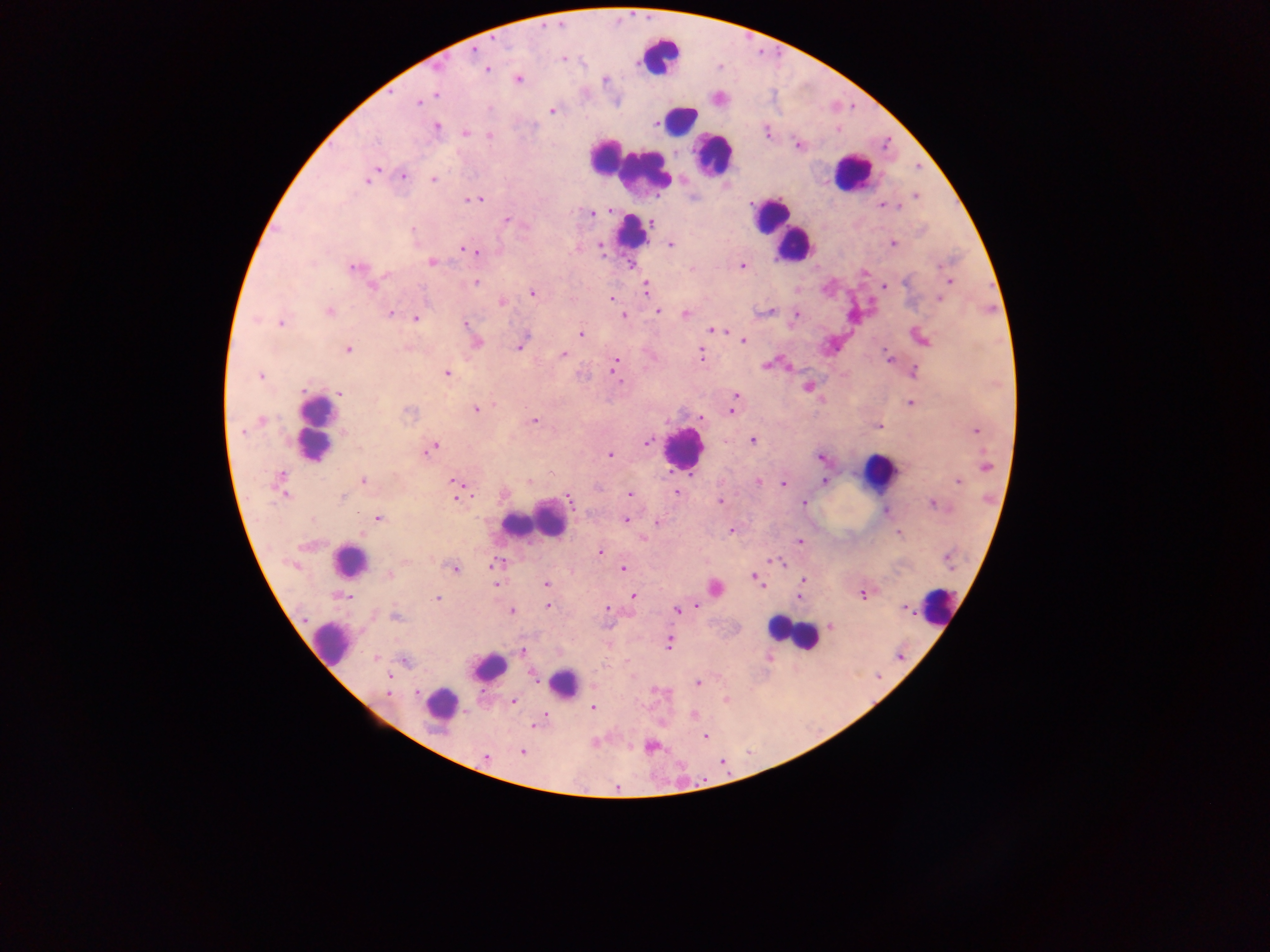
Approximate centers as {x, y} in pixels.
Summary:
  - Leukocyte locations: {660, 56}, {679, 119}, {712, 154}, {609, 157}, {637, 169}, {852, 173}, {770, 214}, {781, 229}, {632, 233}, {793, 245}, {316, 428}, {683, 448}, {878, 472}, {546, 517}, {513, 524}, {349, 561}, {938, 606}, {792, 634}, {329, 642}, {489, 666}, {563, 683}, {440, 704}
  - Plasmodium parasite locations: {474, 50}, {564, 59}, {438, 68}, {486, 69}, {604, 79}, {519, 80}, {437, 96}, {418, 103}, {489, 109}, {552, 110}, {436, 127}, {766, 131}, {464, 133}, {489, 135}, {798, 145}, {377, 168}, {371, 175}, {403, 175}, {433, 179}, {367, 181}, {915, 197}, {466, 199}, {476, 199}, {884, 205}, {896, 207}, {610, 211}, {598, 213}, {592, 214}, {506, 220}, {651, 222}, {413, 230}, {671, 244}, {893, 244}, {601, 246}, {463, 250}, {475, 252}, {431, 262}, {631, 265}, {742, 266}, {355, 268}, {863, 271}, {949, 281}, {475, 283}, {372, 285}, {885, 286}, {646, 288}, {532, 293}, {611, 298}, {939, 298}, {502, 302}, {329, 311}, {658, 311}, {770, 312}, {390, 313}, {686, 314}, {796, 314}, {624, 316}, {416, 318}, {256, 320}, {280, 323}, {466, 324}, {712, 330}, {722, 332}, {581, 334}, {922, 339}, {743, 341}, {477, 342}, {519, 347}, {347, 350}, {563, 354}, {700, 354}, {886, 354}, {889, 358}, {616, 360}, {766, 365}, {614, 368}, {914, 372}, {446, 373}, {260, 376}, {620, 382}, {808, 387}, {340, 394}, {736, 396}, {734, 401}, {910, 402}, {494, 404}, {476, 409}, {732, 410}, {408, 412}, {702, 418}, {261, 420}, {533, 421}, {879, 426}, {976, 430}, {241, 432}, {752, 441}, {647, 443}, {433, 447}, {610, 454}, {821, 458}, {986, 467}, {281, 476}, {364, 481}, {455, 481}, {958, 481}, {529, 482}, {759, 482}, {824, 482}, {782, 484}, {629, 493}, {677, 493}, {286, 495}, {456, 497}, {342, 498}, {570, 499}, {720, 501}, {804, 502}, {931, 504}, {885, 512}, {379, 518}, {625, 520}, {657, 522}, {731, 531}, {899, 534}, {643, 538}, {800, 541}, {601, 552}, {949, 560}, {772, 561}, {779, 563}, {492, 565}, {454, 569}, {623, 569}, {389, 574}, {754, 577}, {757, 581}, {803, 581}, {496, 584}, {546, 585}, {715, 588}, {864, 594}, {634, 595}, {344, 596}, {798, 596}, {437, 599}, {548, 606}, {695, 607}, {607, 609}, {905, 609}, {511, 611}, {677, 611}, {396, 617}, {831, 626}, {668, 644}, {522, 651}, {375, 657}, {406, 661}, {533, 675}, {389, 677}, {698, 683}, {417, 692}, {388, 694}, {726, 699}, {514, 702}, {593, 707}, {695, 715}, {535, 725}, {705, 736}, {651, 746}, {522, 752}, {485, 757}, {617, 788}
  - Capture: mobile-phone photograph through a microscope
  - Image size: 1270×952 pixels
  - Preparation: thick blood smear
  - Country: Ghana
  - Field of view: single